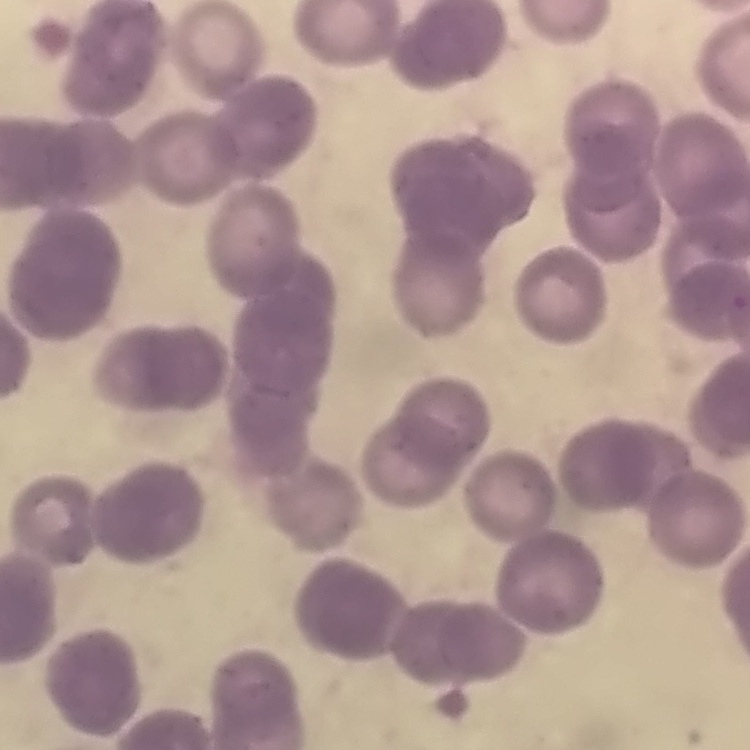
Summary:
  - Red blood cell morphology: rouleaux formation
  - Preparation: thin blood film
  - Stain: Field's or Giemsa
  - Image type: square crop of a larger photomicrograph